Point out each Plasmodium parasite.
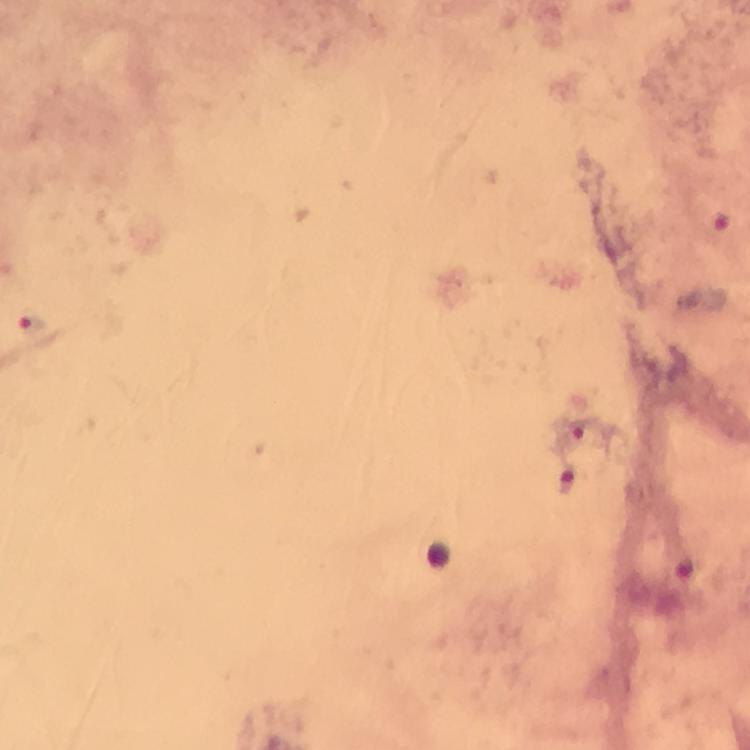

Approximate centers as (x, y) in pixels.
Plasmodium parasites: (723, 224), (31, 322), (566, 481).

100x magnification. Giemsa stain. Photographed with a smartphone mounted on the microscope. A crop from one field of view. Thick smear. Immersion oil applied. Image is 750×750 pixels. From a malaria diagnostic workup.